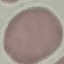 Result: no malaria parasites detected. Photographed with a smartphone camera at the microscope eyepiece. Thin smear of blood. Cell patch, automatically extracted from a larger field of view and resized to 64 × 64 pixels. Giemsa stain.